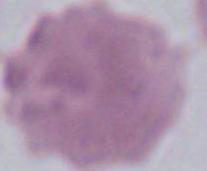

{
  "identification": "erythrocyte",
  "magnification": "1000x",
  "modality": "micrograph"
}